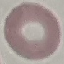 Malaria status: uninfected. Giemsa stain. Automatically extracted cell patch, resized to 64 × 64 pixels. Thin smear of blood. Acquired by smartphone through the microscope eyepiece.